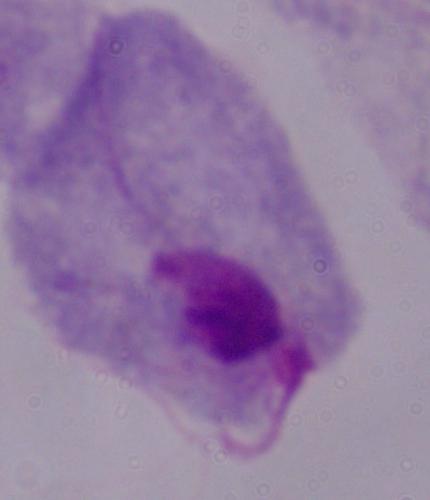
Summary:
  - Modality: photomicrograph
  - Magnification: 1000x
  - Identification: trichomonad